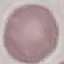 Result: no malaria parasites detected. Thin blood smear. Giemsa stain. Acquired by smartphone through the microscope eyepiece. Cell patch, automatically extracted from a larger field of view and resized to 64 × 64 pixels.